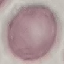
malaria status = uninfected
preparation = thin blood film
image type = automatically extracted cell patch, resized to 64 × 64 pixels
stain = Giemsa
capture = smartphone through the microscope eyepiece